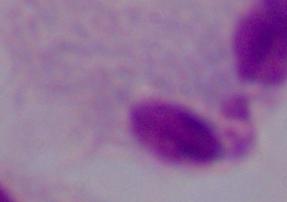

Photomicrograph. 1000x magnification. A trichomonad is shown.